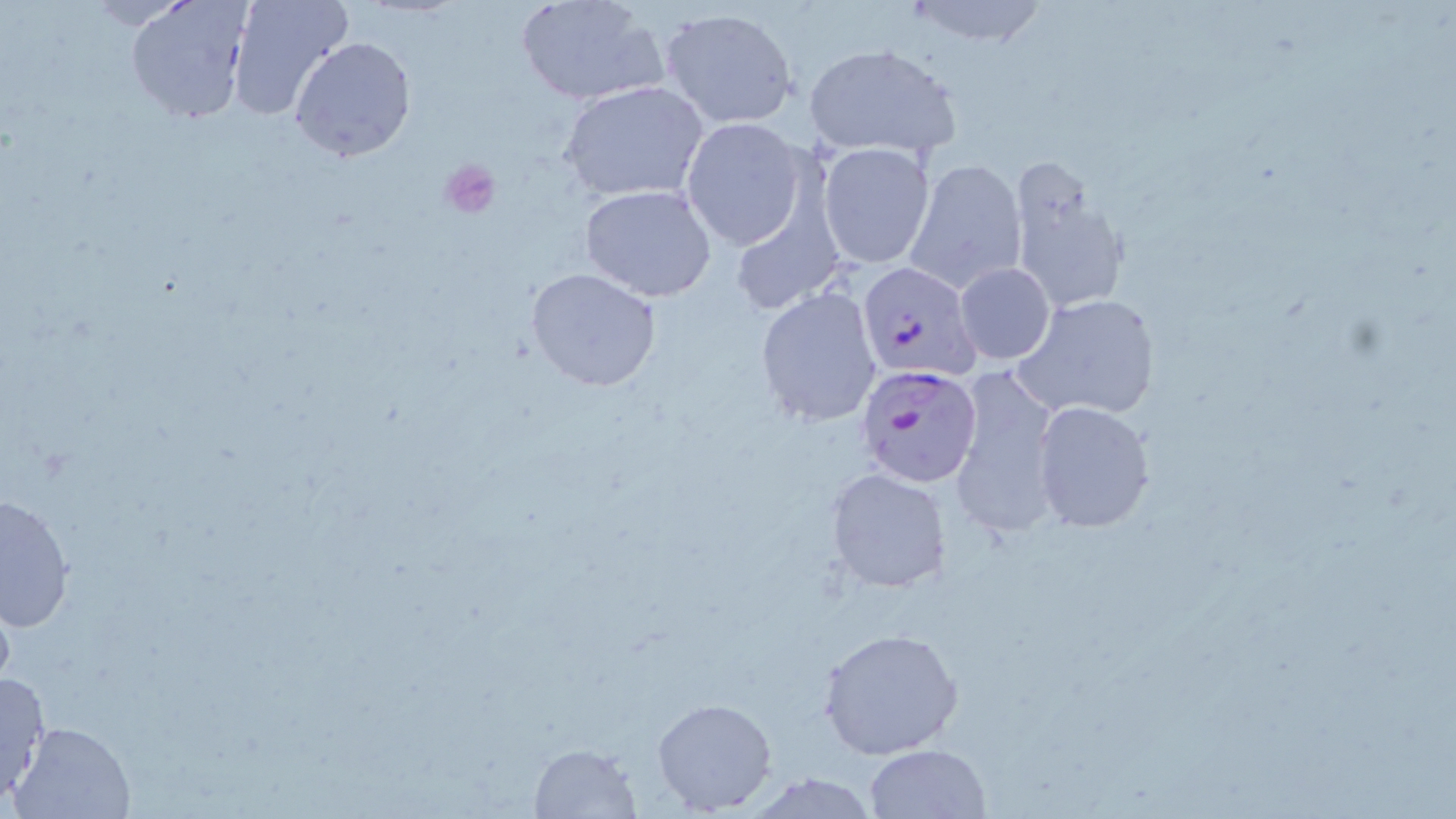

Summary:
  - Coordinate format: approximate bounding boxes as (x1,y1)-(x2,y2) corner pairs in pixels
  - Platelet locations: (439,158)-(501,221)
  - Uninfected red blood cell locations: (225,0)-(354,122), (516,0)-(666,107), (902,0)-(1049,47), (126,1)-(254,125), (660,7)-(799,129), (290,35)-(417,162), (804,42)-(961,162), (562,81)-(710,203), (682,117)-(809,250), (817,143)-(935,269), (1005,154)-(1131,318), (905,159)-(1026,292), (579,184)-(717,301), (954,263)-(1055,365), (525,267)-(661,392), (755,285)-(881,428), (1011,293)-(1163,422), (947,373)-(1062,537), (1031,400)-(1155,533), (825,466)-(951,595), (1,493)-(75,631), (819,626)-(965,761), (0,670)-(52,805), (652,698)-(776,815), (11,721)-(137,818), (526,742)-(644,818), (865,744)-(991,819), (747,773)-(882,817)
  - Plasmodium falciparum-infected red blood cell locations: (858,262)-(981,380), (855,362)-(983,488)
  - Slide-level diagnosis: Plasmodium falciparum
  - Preparation: thin blood smear
  - Magnification: 1000x
  - Modality: optical microscopy
  - Field of view: single
  - Image size: 1456×819 pixels
  - Stain: May-Grünwald-Giemsa